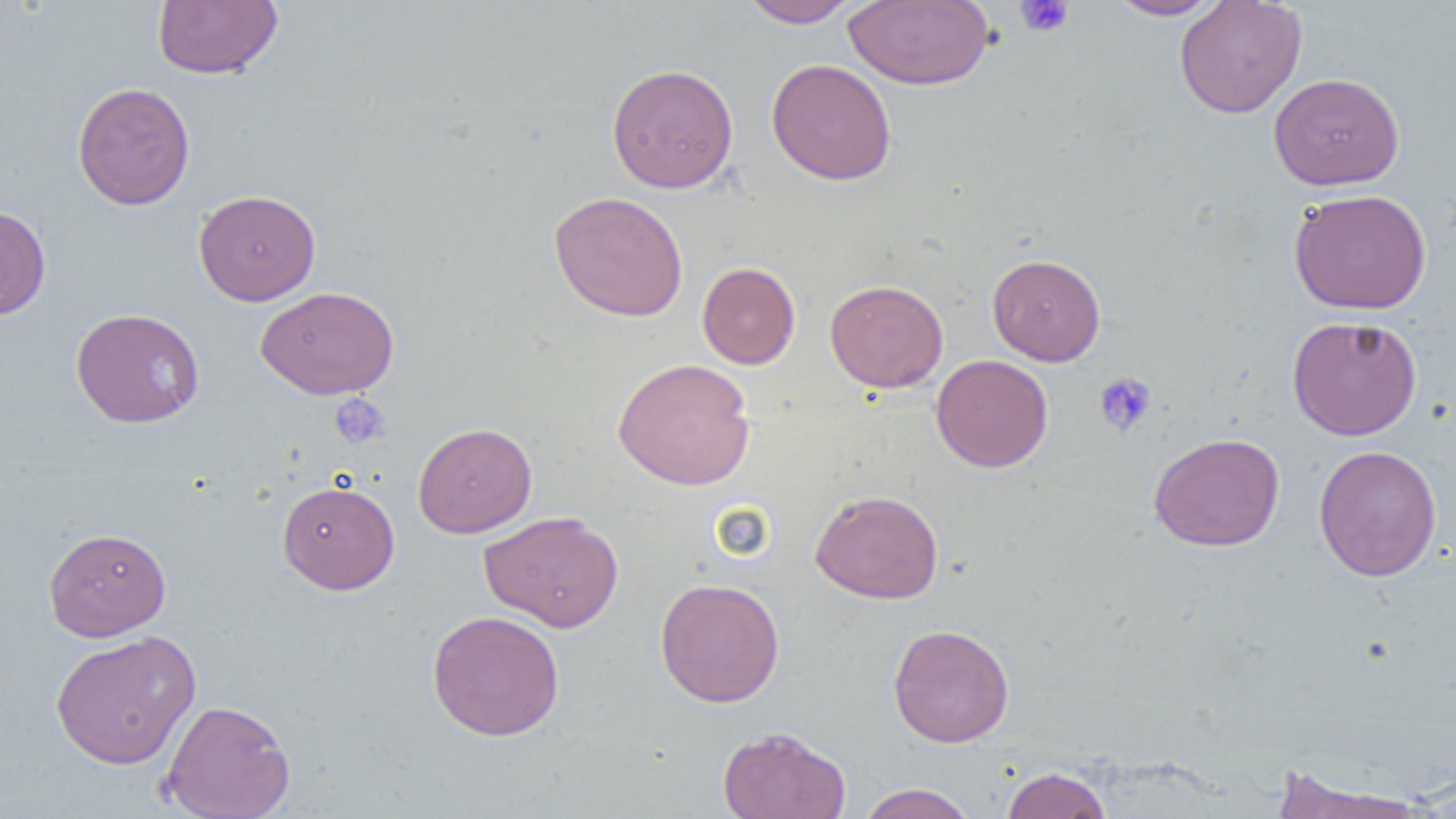
Summary:
  - Coordinate format: approximate bounding boxes as named x1/y1/x2/y2 corners in pixels
  - Platelet locations: (x1=1014, y1=0, x2=1075, y2=38), (x1=1093, y1=371, x2=1157, y2=437), (x1=330, y1=394, x2=390, y2=449)
  - Uninfected red blood cell locations: (x1=153, y1=0, x2=282, y2=80), (x1=739, y1=0, x2=861, y2=28), (x1=1107, y1=0, x2=1226, y2=20), (x1=845, y1=1, x2=994, y2=89), (x1=1174, y1=1, x2=1307, y2=118), (x1=767, y1=58, x2=897, y2=185), (x1=607, y1=63, x2=739, y2=193), (x1=1269, y1=71, x2=1404, y2=190), (x1=72, y1=82, x2=195, y2=210), (x1=194, y1=189, x2=321, y2=305), (x1=1289, y1=189, x2=1431, y2=314), (x1=548, y1=191, x2=688, y2=321), (x1=0, y1=205, x2=51, y2=319), (x1=987, y1=253, x2=1106, y2=365), (x1=697, y1=261, x2=800, y2=369), (x1=824, y1=279, x2=948, y2=392), (x1=255, y1=285, x2=399, y2=399), (x1=70, y1=307, x2=204, y2=429), (x1=1287, y1=315, x2=1422, y2=440), (x1=931, y1=354, x2=1053, y2=472), (x1=613, y1=357, x2=755, y2=490), (x1=412, y1=422, x2=537, y2=538), (x1=1148, y1=432, x2=1285, y2=552), (x1=1314, y1=445, x2=1442, y2=582), (x1=277, y1=479, x2=399, y2=594), (x1=810, y1=489, x2=944, y2=604), (x1=479, y1=510, x2=624, y2=632), (x1=44, y1=527, x2=171, y2=641), (x1=655, y1=577, x2=785, y2=707), (x1=427, y1=610, x2=565, y2=741), (x1=888, y1=624, x2=1014, y2=747), (x1=49, y1=629, x2=202, y2=768), (x1=161, y1=698, x2=295, y2=819), (x1=717, y1=725, x2=852, y2=819), (x1=1001, y1=767, x2=1110, y2=818), (x1=1271, y1=768, x2=1430, y2=819), (x1=857, y1=783, x2=977, y2=819)
  - Slide-level diagnosis: no evidence of blood parasites
  - Preparation: thin blood smear
  - Modality: optical microscopy
  - Magnification: 1000x
  - Image size: 1456×819 pixels
  - Field of view: single